Name the parasite shown.
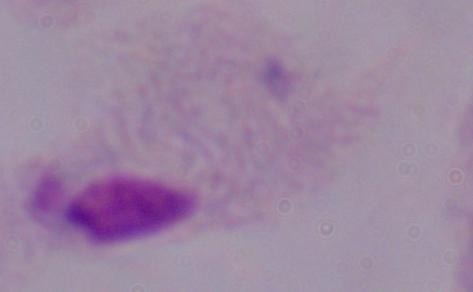
This is a trichomonad.

magnification = 1000x
modality = photomicrograph